Comment on the morphology of the red blood cells.
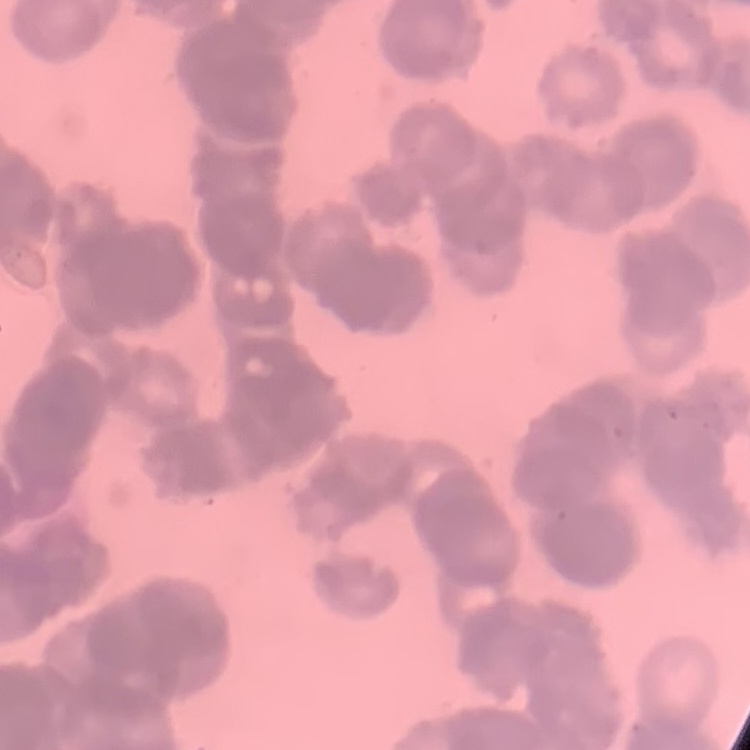
Rouleaux formation.

{
  "image_type": "square crop of a larger photomicrograph",
  "preparation": "thin blood film",
  "stain": "Field's or Giemsa"
}